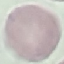
Malaria status: uninfected. Acquired by smartphone through the microscope eyepiece. Automatically extracted cell patch, resized to 64 × 64 pixels. Thin blood film. Giemsa stain.